Locate every white blood cell.
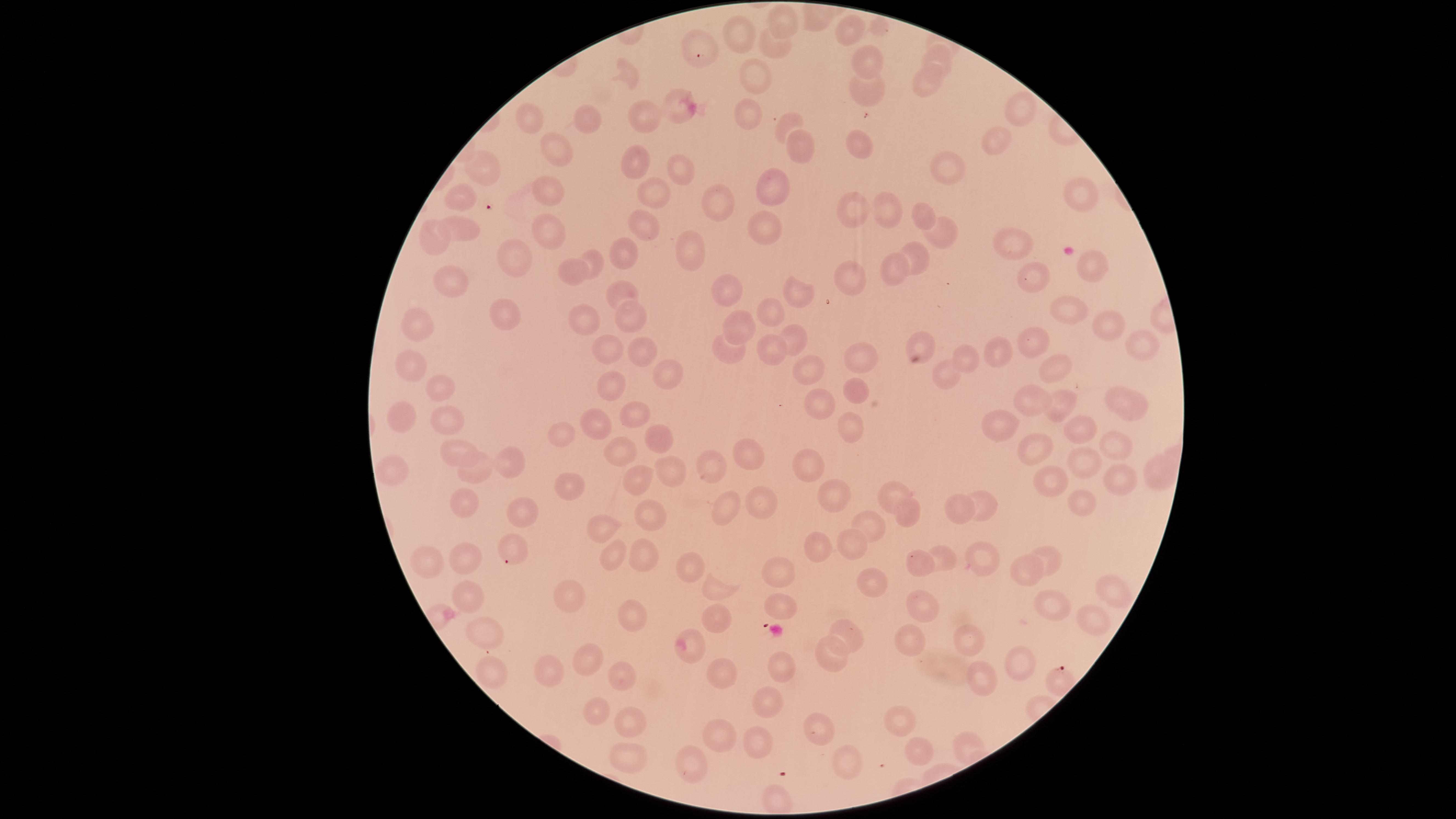
No white blood cells identified.

Approximate marker points as {x, y} in pixels.
Summary:
  - Uninfected red blood cells: {780, 18}, {742, 28}, {849, 29}, {693, 42}, {769, 48}, {938, 61}, {875, 65}, {625, 73}, {751, 77}, {926, 84}, {866, 90}, {676, 109}, {1019, 110}, {745, 114}, {649, 116}, {534, 121}, {588, 123}, {788, 123}, {995, 142}, {863, 146}, {559, 150}, {800, 150}, {631, 161}, {943, 170}, {680, 171}, {480, 174}, {775, 183}, {551, 193}, {657, 194}, {1079, 194}, {460, 199}, {718, 205}, {887, 210}, {854, 212}, {919, 215}, {648, 221}, {767, 225}, {462, 228}, {551, 234}, {943, 235}, {438, 237}, {689, 242}, {1016, 245}, {619, 251}, {593, 258}, {919, 259}, {1091, 259}, {512, 262}, {894, 268}, {853, 273}, {572, 274}, {1028, 282}, {452, 283}, {621, 288}, {728, 289}, {801, 294}, {770, 310}, {1070, 311}, {507, 313}, {629, 316}, {584, 321}, {1107, 324}, {423, 326}, {743, 329}, {797, 342}, {1034, 342}, {1139, 343}, {772, 346}, {922, 347}, {614, 348}, {729, 348}, {638, 351}, {997, 352}, {964, 354}, {861, 359}, {412, 364}, {660, 369}, {1057, 369}, {809, 372}, {944, 376}, {609, 389}, {443, 391}, {856, 392}, {1122, 399}, {1029, 401}, {823, 407}, {1058, 408}, {631, 415}, {446, 416}, {399, 417}, {592, 425}, {851, 426}, {996, 428}, {1074, 428}, {655, 432}, {563, 435}, {1116, 447}, {1039, 450}, {619, 452}, {749, 454}, {455, 458}, {506, 462}, {1086, 462}, {670, 463}, {808, 466}, {394, 470}, {711, 470}, {481, 471}, {1155, 471}, {1124, 478}, {1046, 480}, {631, 482}, {566, 488}, {826, 493}, {892, 495}, {461, 503}, {760, 503}, {1081, 503}, {965, 506}, {726, 507}, {987, 507}, {519, 515}, {905, 516}, {646, 519}, {870, 527}, {596, 529}, {512, 540}, {812, 547}, {853, 548}, {975, 551}, {610, 555}, {639, 557}, {431, 559}, {1045, 559}, {469, 562}, {941, 562}, {692, 563}, {921, 563}, {1021, 572}, {777, 575}, {869, 576}, {715, 591}, {1110, 591}, {471, 597}, {562, 597}, {779, 604}, {925, 605}, {1047, 606}, {1091, 617}, {631, 618}, {715, 624}, {848, 631}, {489, 633}, {965, 635}, {910, 640}, {692, 643}, {831, 653}, {1018, 656}, {585, 657}, {778, 661}, {489, 670}, {614, 672}, {551, 673}, {978, 675}, {721, 677}, {769, 701}, {594, 713}, {632, 720}, {893, 723}, {818, 735}, {722, 740}, {757, 744}, {918, 750}, {627, 754}, {692, 766}, {851, 766}, {772, 799}
  - Stain: Giemsa
  - Field of view: single
  - Presence: no malaria parasites detected
  - Capture: smartphone photograph through the microscope eyepiece
  - Image size: 1456×819 pixels
  - Visible region: circular
  - Preparation: thin blood film